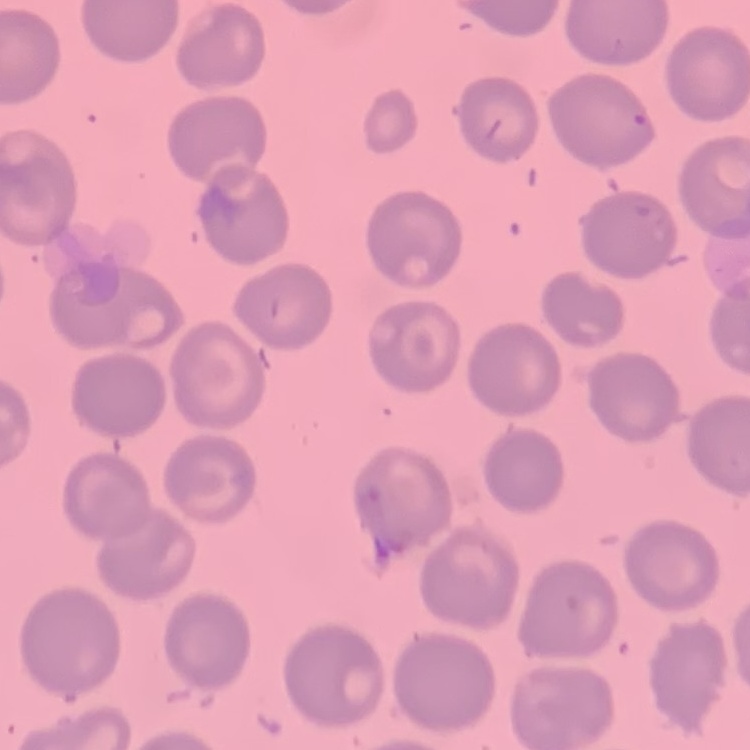

The erythrocytes show no rouleaux formation. Thin peripheral smear. One tile cut from a larger photomicrograph. Field's or Giemsa stain.